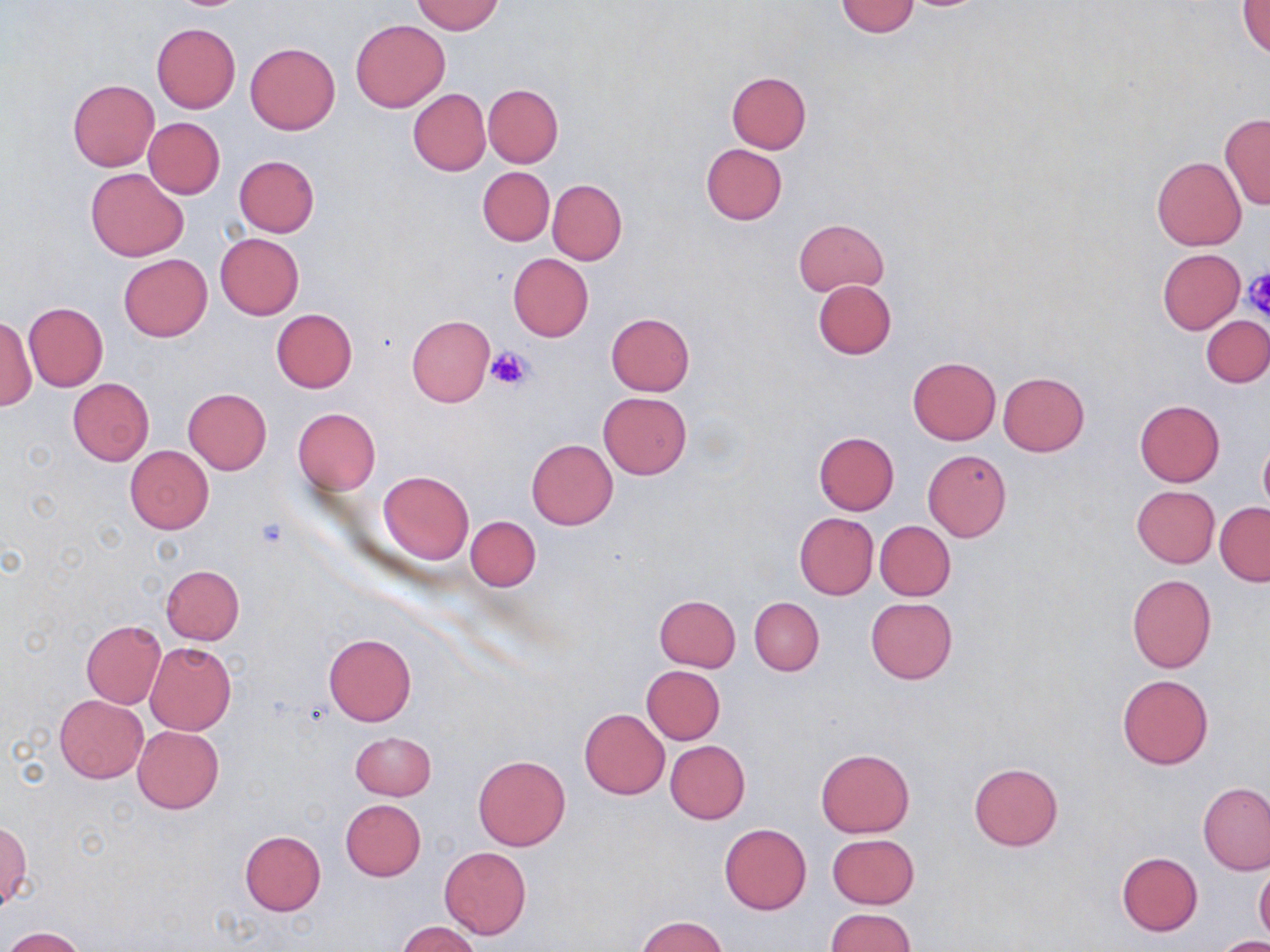

slide-level diagnosis = no evidence of blood parasites
uninfected red blood cell locations = approximate bounding boxes as named x1/y1/x2/y2 corners in pixels: (x1=412, y1=1, x2=504, y2=35), (x1=834, y1=1, x2=919, y2=37), (x1=1240, y1=2, x2=1270, y2=57), (x1=351, y1=20, x2=450, y2=111), (x1=151, y1=23, x2=240, y2=112), (x1=245, y1=42, x2=339, y2=134), (x1=726, y1=71, x2=811, y2=153), (x1=68, y1=81, x2=159, y2=171), (x1=482, y1=84, x2=563, y2=167), (x1=407, y1=89, x2=490, y2=175), (x1=1219, y1=113, x2=1270, y2=210), (x1=143, y1=117, x2=225, y2=198), (x1=700, y1=144, x2=787, y2=225), (x1=228, y1=155, x2=311, y2=319), (x1=234, y1=155, x2=319, y2=237), (x1=1152, y1=156, x2=1247, y2=250), (x1=478, y1=166, x2=555, y2=246), (x1=86, y1=168, x2=188, y2=261), (x1=547, y1=180, x2=627, y2=264), (x1=794, y1=218, x2=888, y2=295), (x1=215, y1=233, x2=303, y2=319), (x1=1157, y1=247, x2=1245, y2=335), (x1=118, y1=253, x2=212, y2=342), (x1=508, y1=253, x2=594, y2=341), (x1=812, y1=280, x2=896, y2=360), (x1=24, y1=304, x2=108, y2=390), (x1=271, y1=309, x2=357, y2=394), (x1=606, y1=312, x2=695, y2=396), (x1=1, y1=315, x2=36, y2=411), (x1=406, y1=315, x2=495, y2=406), (x1=1202, y1=316, x2=1270, y2=387), (x1=908, y1=357, x2=1000, y2=445), (x1=998, y1=372, x2=1089, y2=455), (x1=68, y1=378, x2=154, y2=466), (x1=183, y1=388, x2=272, y2=474), (x1=599, y1=392, x2=692, y2=479), (x1=1134, y1=399, x2=1224, y2=486), (x1=292, y1=408, x2=380, y2=493), (x1=813, y1=431, x2=899, y2=515), (x1=526, y1=439, x2=619, y2=530), (x1=1258, y1=440, x2=1270, y2=513), (x1=124, y1=446, x2=215, y2=534), (x1=923, y1=450, x2=1012, y2=541), (x1=378, y1=470, x2=474, y2=564), (x1=1132, y1=486, x2=1219, y2=567), (x1=1215, y1=502, x2=1270, y2=585), (x1=794, y1=513, x2=878, y2=600), (x1=466, y1=515, x2=540, y2=591), (x1=876, y1=521, x2=955, y2=600), (x1=161, y1=565, x2=244, y2=644), (x1=1127, y1=573, x2=1217, y2=673), (x1=654, y1=594, x2=741, y2=672), (x1=750, y1=597, x2=824, y2=676), (x1=866, y1=597, x2=957, y2=684), (x1=81, y1=620, x2=166, y2=708), (x1=323, y1=632, x2=416, y2=725), (x1=145, y1=642, x2=237, y2=734), (x1=641, y1=665, x2=726, y2=744), (x1=1117, y1=674, x2=1213, y2=770), (x1=54, y1=695, x2=147, y2=782), (x1=578, y1=708, x2=669, y2=800), (x1=133, y1=725, x2=224, y2=813), (x1=350, y1=731, x2=435, y2=800), (x1=666, y1=741, x2=751, y2=823), (x1=815, y1=748, x2=915, y2=837), (x1=473, y1=755, x2=570, y2=851), (x1=969, y1=762, x2=1063, y2=850), (x1=1199, y1=782, x2=1269, y2=875), (x1=341, y1=799, x2=426, y2=880), (x1=2, y1=822, x2=31, y2=913), (x1=720, y1=823, x2=812, y2=914), (x1=240, y1=830, x2=326, y2=915), (x1=827, y1=834, x2=920, y2=909), (x1=439, y1=846, x2=532, y2=939), (x1=1117, y1=852, x2=1203, y2=935), (x1=1254, y1=863, x2=1270, y2=944), (x1=826, y1=908, x2=914, y2=952), (x1=634, y1=915, x2=728, y2=952), (x1=398, y1=921, x2=482, y2=952), (x1=1, y1=926, x2=87, y2=952), (x1=1213, y1=937, x2=1270, y2=952)
field of view = single
platelet locations = approximate bounding boxes as named x1/y1/x2/y2 corners in pixels: (x1=1244, y1=269, x2=1269, y2=320), (x1=486, y1=347, x2=535, y2=392)
stain = May-Grünwald-Giemsa
magnification = 1000x
image size = 1270×952 pixels
modality = optical microscopy
preparation = thin blood film